Give the position of every malaria parasite, noting whether each is a trophozoite, schizont, or gametocyte.
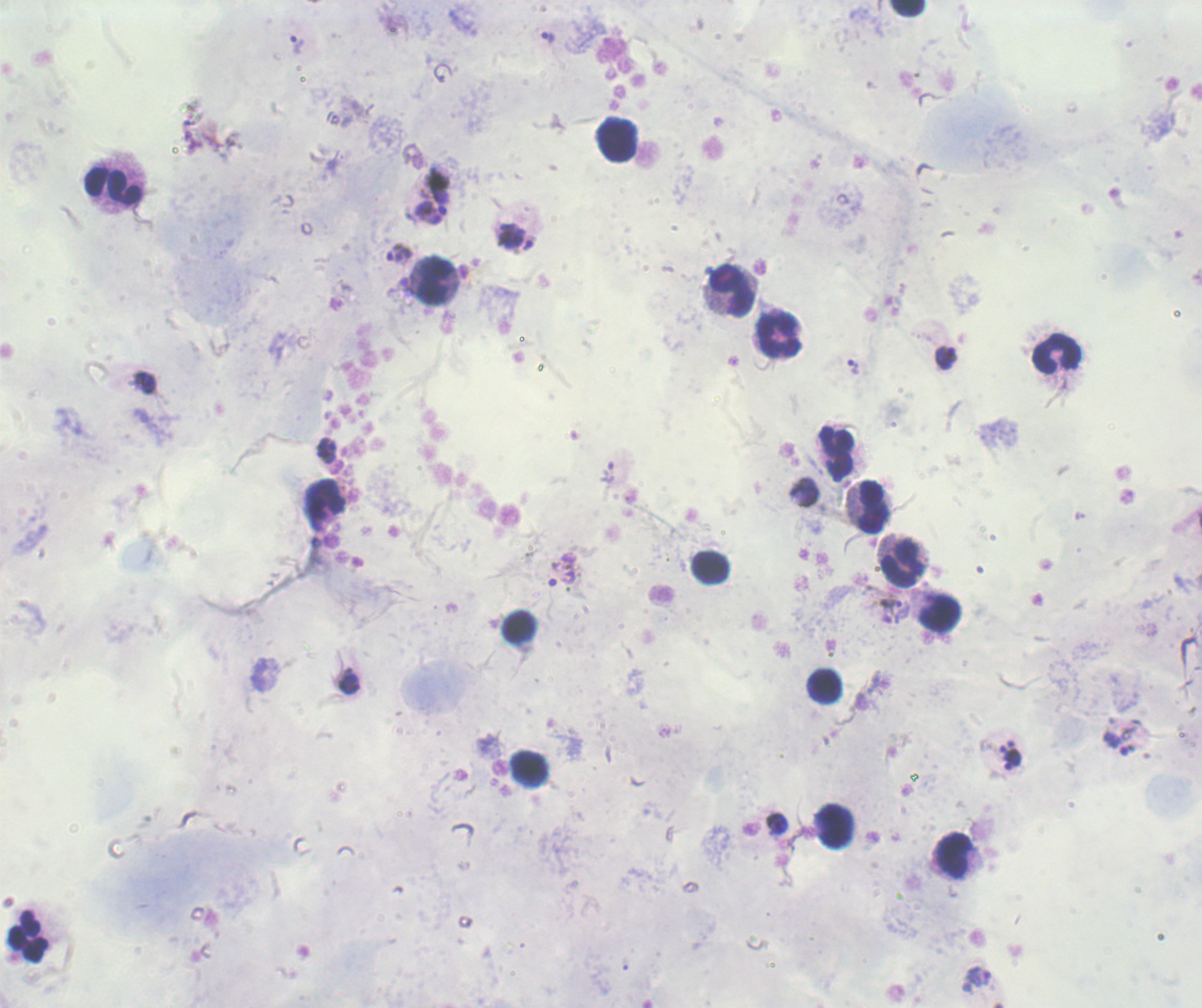
Approximate object centers, in pixels from the top-left corner.
Trophozoites: (x=548, y=37), (x=297, y=43), (x=432, y=205), (x=399, y=252), (x=946, y=357), (x=853, y=365), (x=145, y=383), (x=328, y=444), (x=326, y=457), (x=563, y=571), (x=890, y=602), (x=348, y=684), (x=1011, y=760).
Schizonts: (x=515, y=237).
No gametocyte forms observed.

image_size: 1202×1008 pixels
context: previously used in a real diagnosis
stain: Romanowsky
field_of_view: single
magnification: 100x
background_quality: unsatisfactory
preparation: thick smear of blood
leukocyte_locations: 'approximate object centers, in pixels from the top-left corner: (x=908, y=8), (x=620, y=140), (x=114, y=182), (x=435, y=282), (x=729, y=290), (x=775, y=334), (x=1056, y=355), (x=839, y=454), (x=324, y=499), (x=870, y=506), (x=902, y=563), (x=712, y=569), (x=940, y=614), (x=519, y=629), (x=826, y=687), (x=530, y=770), (x=832, y=826), (x=952, y=854), (x=28, y=935)'